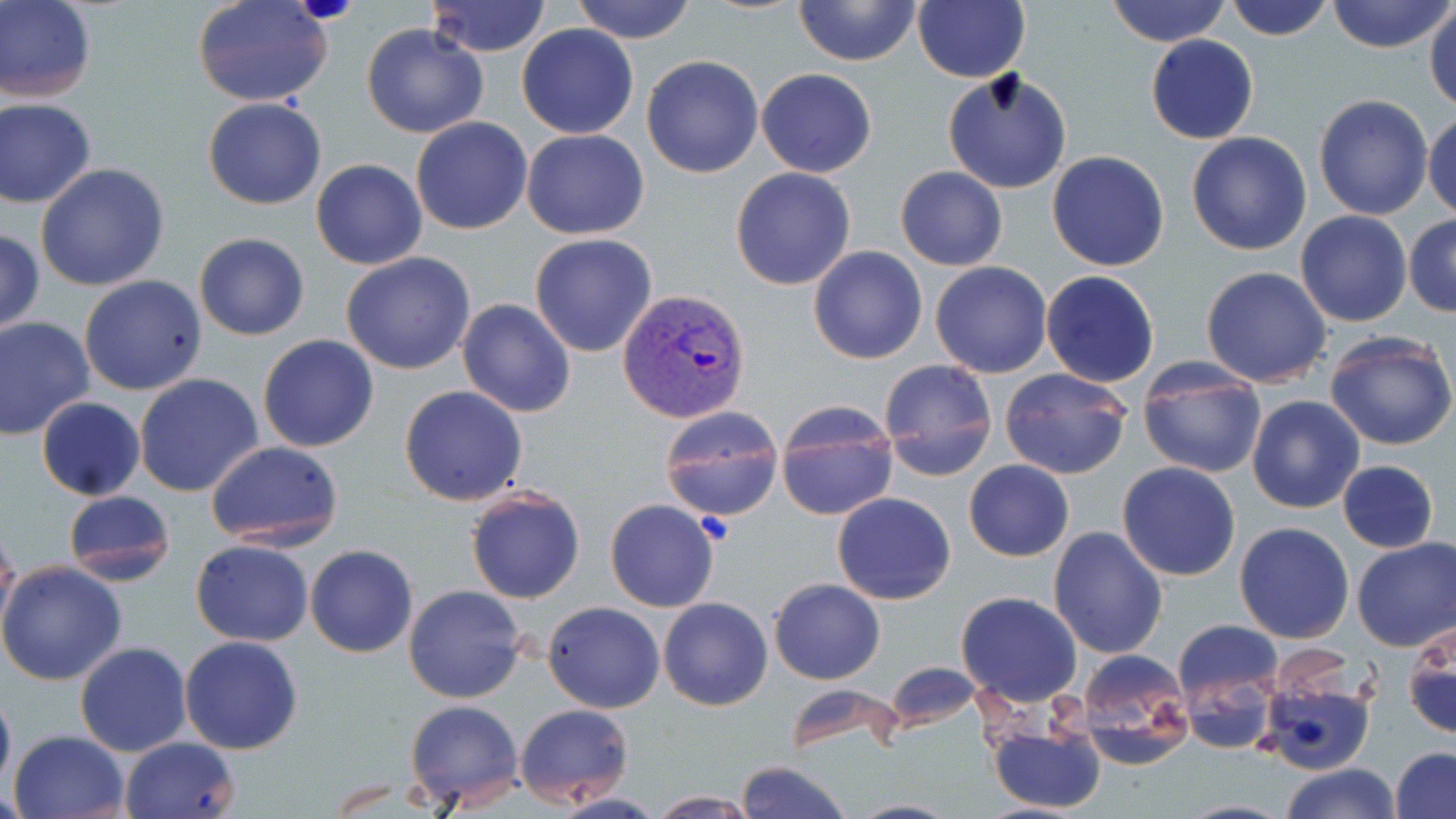
Approximate bounding boxes as (x1, y1, x2, y2) in pixels. Platelet locations: (294, 0, 357, 24). Plasmodium vivax-infected red blood cell locations: (617, 285, 752, 421). Uninfected red blood cell locations: (0, 0, 97, 103), (425, 0, 553, 57), (571, 0, 697, 44), (794, 0, 921, 67), (914, 0, 1029, 83), (1105, 0, 1231, 47), (1224, 0, 1335, 41), (1328, 0, 1453, 53), (193, 1, 335, 108), (1425, 2, 1456, 114), (361, 24, 489, 138), (516, 24, 638, 139), (1146, 34, 1258, 144), (641, 55, 764, 177), (755, 67, 877, 177), (942, 68, 1072, 194), (1313, 94, 1434, 221), (203, 98, 327, 209), (0, 100, 98, 208), (1424, 110, 1456, 222), (411, 116, 532, 235), (522, 128, 649, 240), (1186, 131, 1312, 256), (1047, 150, 1170, 272), (311, 159, 427, 270), (35, 163, 170, 292), (895, 166, 1007, 271), (730, 167, 856, 290), (1295, 210, 1412, 328), (1403, 214, 1456, 317), (0, 228, 45, 337), (194, 232, 309, 341), (529, 233, 658, 358), (809, 246, 928, 365), (341, 253, 476, 374), (930, 261, 1052, 378), (1200, 266, 1333, 387), (1041, 271, 1159, 388), (79, 274, 207, 396), (457, 299, 576, 419), (0, 316, 95, 440), (1324, 330, 1456, 451), (258, 335, 380, 454), (877, 357, 997, 480), (1136, 358, 1268, 478), (999, 367, 1132, 479), (134, 374, 264, 498), (400, 385, 528, 506), (36, 395, 145, 500), (1246, 395, 1365, 513), (774, 400, 898, 520), (658, 405, 784, 523), (206, 440, 344, 550), (964, 460, 1073, 561), (1336, 460, 1438, 553), (1116, 462, 1242, 582), (466, 488, 584, 605), (62, 490, 177, 585), (832, 492, 955, 605), (605, 499, 720, 613), (1234, 521, 1356, 643), (0, 525, 22, 637), (1048, 526, 1168, 660), (1351, 537, 1456, 653), (191, 540, 314, 646), (305, 544, 417, 658), (0, 560, 127, 686), (769, 578, 886, 685), (404, 584, 527, 703), (956, 592, 1081, 707), (658, 597, 772, 711), (543, 602, 665, 713), (1403, 618, 1455, 742), (1173, 620, 1285, 728), (179, 636, 304, 754), (75, 642, 192, 756), (1072, 648, 1196, 769), (884, 661, 982, 732), (1255, 674, 1376, 775), (0, 684, 16, 795), (404, 697, 526, 806), (515, 703, 634, 808), (985, 713, 1108, 816), (7, 729, 130, 819), (120, 736, 240, 819), (1389, 746, 1456, 819), (735, 760, 853, 819), (1279, 762, 1402, 819), (550, 792, 671, 819), (644, 792, 760, 817), (845, 798, 963, 818). Slide-level diagnosis: Plasmodium vivax. Thin blood smear. Optical microscopy. One field of a larger specimen. Captured at 1000x magnification. May-Grünwald-Giemsa stain. Image is 1456×819 pixels.